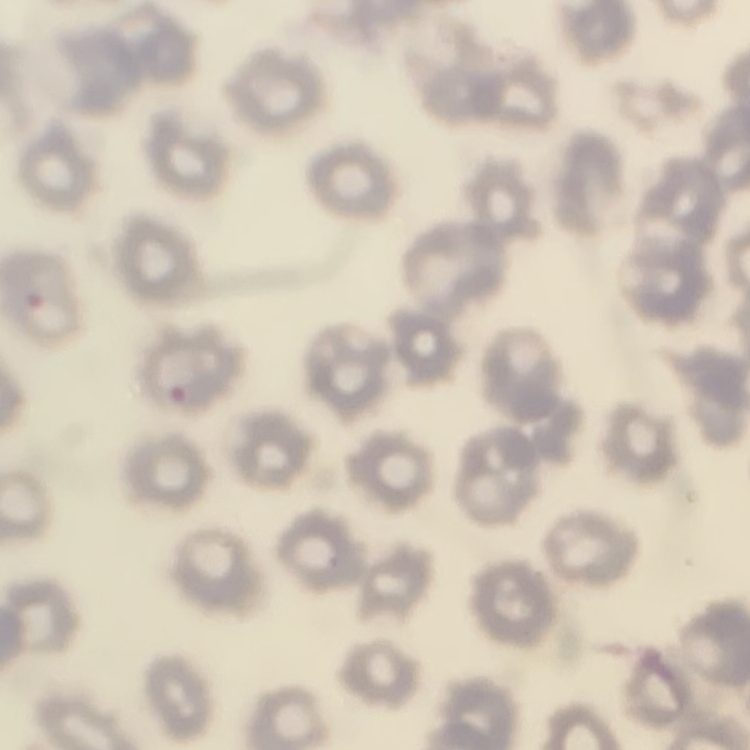
erythrocyte morphology = no rouleaux formation
preparation = thin blood film
stain = Field's or Giemsa
image type = one tile cut from a larger photomicrograph